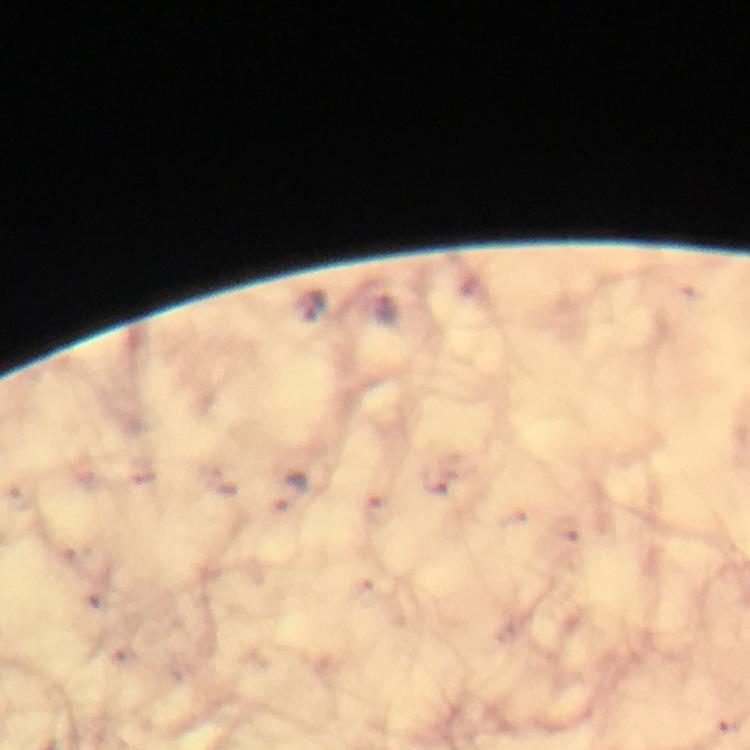

Approximate centers as [x, y] in pixels. Malaria parasite locations: [313, 306], [385, 310], [292, 494]. Giemsa stain. Cropped region of a single field of view. Image is 750×750 pixels. Thick blood smear. Photographed with a smartphone mounted on the microscope. From a malaria diagnostic workup. At 100x magnification. Immersion oil was used.